State which parasite is depicted.
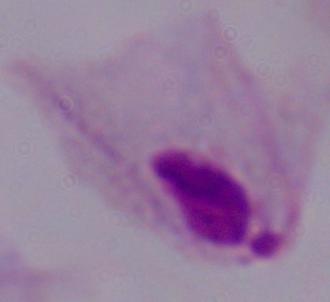

This is a trichomonad.

modality: photomicrograph
magnification: 1000x